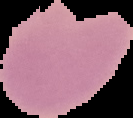
Summary:
  - Result: no Plasmodium parasites detected
  - Image type: segmented cell region with the area outside set to black
  - Image size: 133×118 pixels
  - Preparation: thin blood film